Locate every Plasmodium vivax-infected red blood cell.
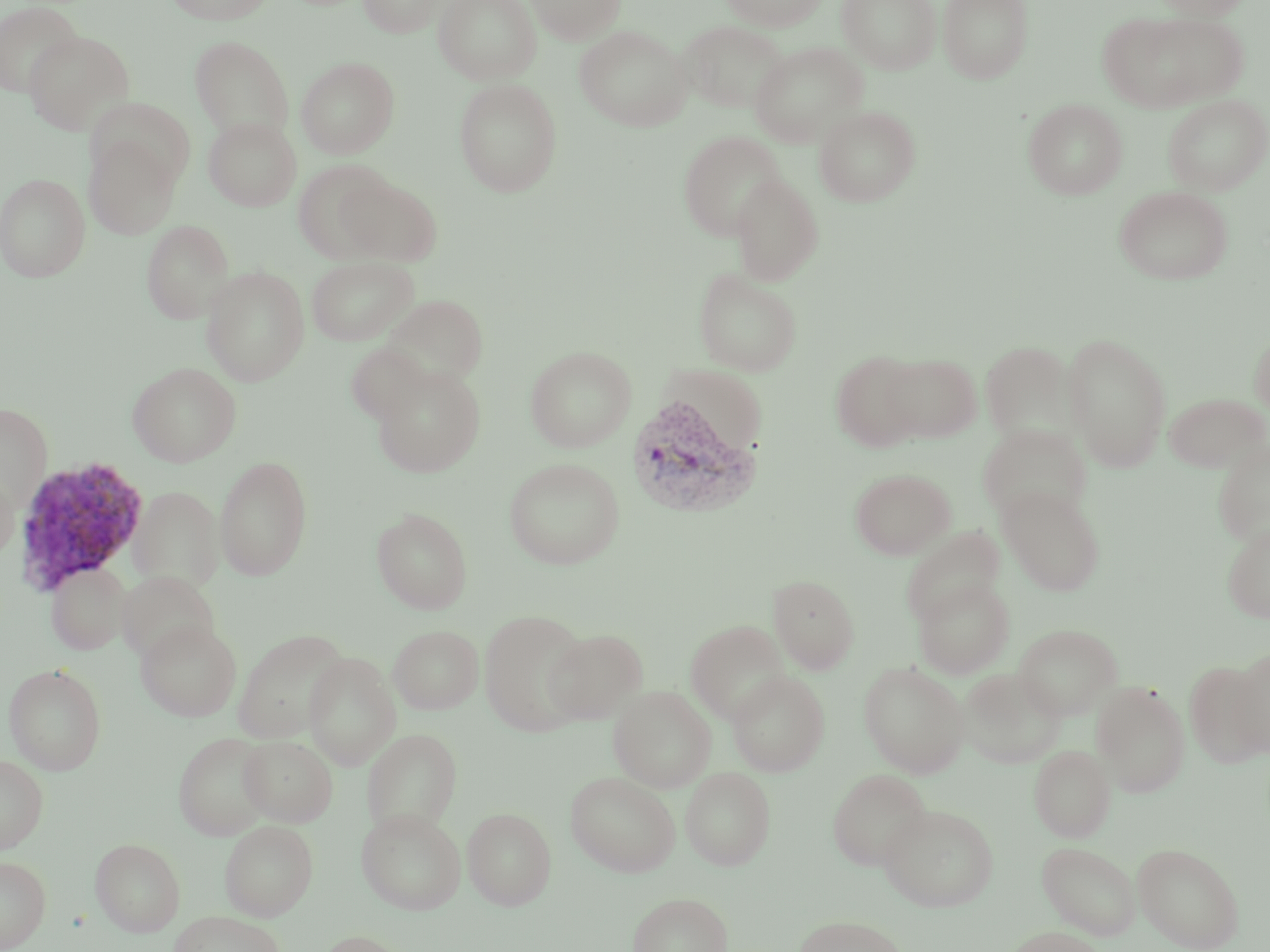

Approximate bounding boxes as (x1, y1, x2, y2) in pixels.
Plasmodium vivax-infected red blood cells: (624, 394, 762, 519), (13, 455, 150, 594).

{
  "slide_level_diagnosis": "Plasmodium vivax",
  "magnification": "1000x",
  "preparation": "thin blood film",
  "image_size": "1270×952 pixels",
  "modality": "optical microscopy",
  "field_of_view": "one of a larger specimen",
  "stain": "May-Grünwald-Giemsa",
  "uninfected_red_blood_cell_locations": "approximate bounding boxes as (x1, y1, x2, y2) in pixels: (165, 0, 276, 25), (358, 0, 448, 37), (432, 0, 541, 84), (525, 0, 626, 44), (720, 0, 828, 31), (837, 0, 941, 74), (937, 0, 1033, 83), (1151, 0, 1251, 20), (0, 1, 83, 99), (1100, 12, 1247, 113), (679, 20, 787, 113), (574, 25, 693, 131), (23, 30, 133, 135), (190, 36, 294, 140), (749, 42, 868, 146), (296, 56, 400, 159), (453, 78, 563, 197), (1163, 94, 1269, 195), (89, 98, 197, 192), (1023, 98, 1127, 199), (813, 105, 920, 206), (203, 117, 301, 211), (678, 131, 786, 240), (84, 135, 181, 239), (293, 160, 396, 262), (0, 172, 90, 282), (730, 173, 824, 284), (338, 176, 442, 266), (1114, 186, 1234, 284), (142, 220, 234, 324), (307, 256, 418, 346), (201, 266, 310, 386), (693, 268, 802, 376), (382, 294, 488, 388), (1249, 327, 1270, 419), (1062, 332, 1172, 472), (979, 340, 1079, 446), (346, 342, 433, 425), (525, 346, 636, 451), (830, 351, 925, 453), (881, 353, 981, 442), (127, 362, 242, 467), (370, 365, 486, 477), (1163, 392, 1269, 472), (0, 403, 52, 510), (977, 424, 1092, 524), (1211, 439, 1270, 547), (215, 456, 312, 581), (504, 458, 625, 569), (0, 467, 19, 562), (850, 468, 955, 560), (130, 486, 224, 591), (997, 486, 1105, 596), (372, 509, 472, 614), (1220, 522, 1270, 624), (900, 528, 1005, 626), (46, 562, 133, 654), (118, 570, 219, 663), (768, 574, 859, 674), (913, 577, 1015, 678), (480, 609, 592, 736), (686, 619, 790, 723), (136, 620, 242, 721), (1013, 623, 1122, 719), (388, 625, 484, 714), (233, 628, 349, 742), (543, 628, 648, 723), (1230, 649, 1270, 758), (304, 653, 400, 770), (1183, 659, 1268, 768), (859, 661, 970, 776), (3, 663, 106, 775), (957, 668, 1067, 769), (727, 670, 830, 776), (1091, 682, 1191, 797), (609, 686, 716, 792), (363, 728, 462, 834), (173, 732, 274, 840), (238, 735, 337, 826), (1029, 744, 1115, 842), (0, 755, 48, 853), (680, 767, 776, 870), (828, 769, 931, 869), (565, 770, 681, 876), (879, 804, 998, 911), (463, 807, 556, 910), (356, 808, 466, 914), (220, 820, 318, 920), (90, 838, 185, 937), (1037, 841, 1141, 940), (1132, 842, 1245, 952), (0, 855, 51, 951), (627, 891, 732, 952), (167, 911, 286, 952), (795, 915, 908, 952), (1004, 927, 1106, 952), (315, 930, 411, 952)"
}